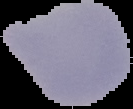

image size = 133×109 pixels
malaria status = uninfected
image type = segmented cell region on a black background
preparation = thin blood film